Assess this cell for malaria.
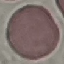

Uninfected.

image type = automatically extracted cell patch, resized to 64 × 64 pixels
preparation = thin blood film
capture = smartphone camera at the microscope eyepiece
stain = Giemsa